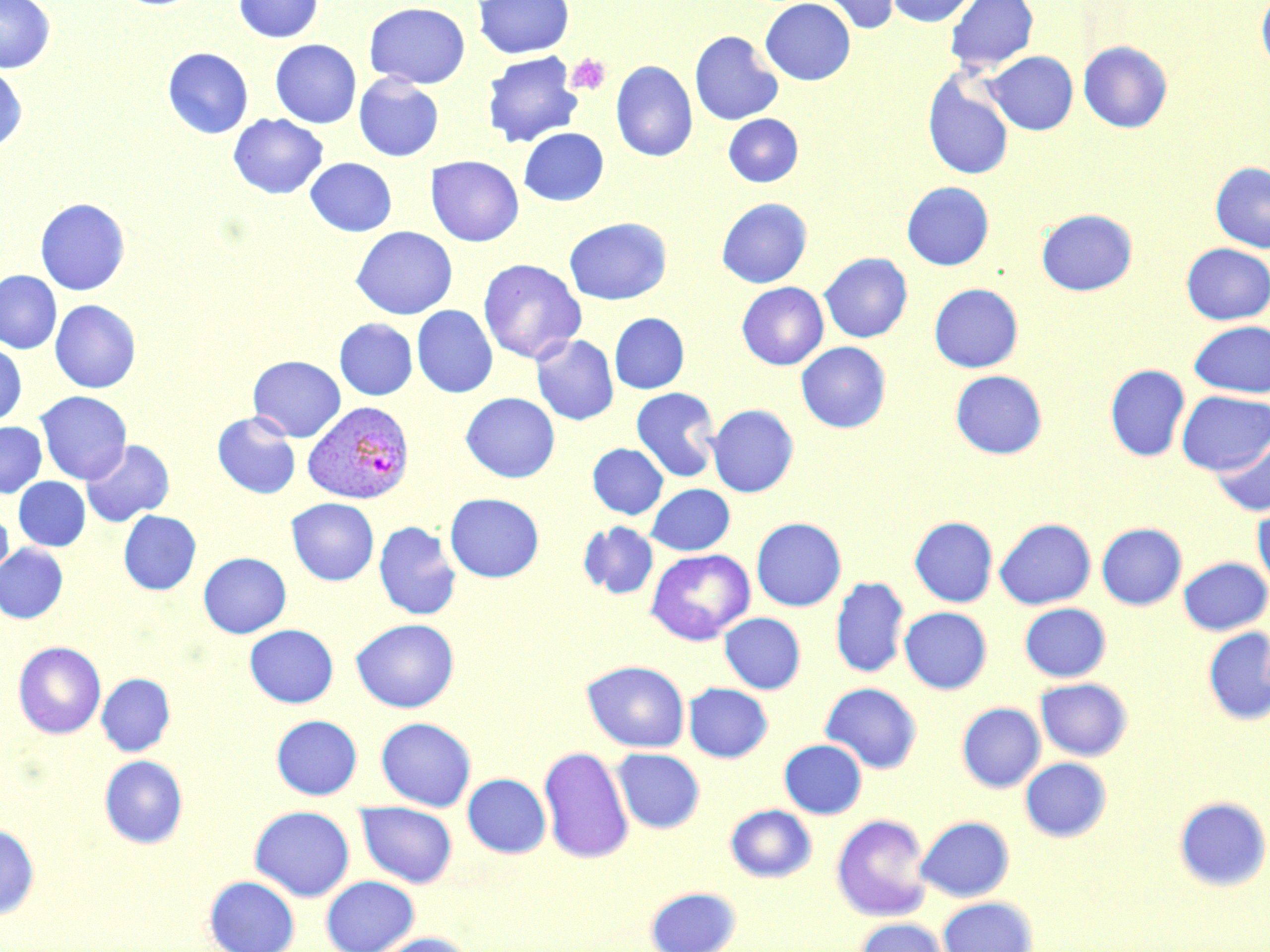
Summary:
  - Coordinate format: approximate bounding boxes as named x1/y1/x2/y2 corners in pixels
  - Platelet locations: (x1=565, y1=53, x2=612, y2=95)
  - Uninfected red blood cell locations: (x1=0, y1=0, x2=55, y2=73), (x1=232, y1=0, x2=323, y2=42), (x1=473, y1=0, x2=574, y2=58), (x1=760, y1=0, x2=855, y2=85), (x1=816, y1=0, x2=901, y2=35), (x1=885, y1=0, x2=977, y2=27), (x1=944, y1=0, x2=1039, y2=74), (x1=1256, y1=0, x2=1270, y2=72), (x1=364, y1=2, x2=471, y2=88), (x1=689, y1=30, x2=784, y2=125), (x1=270, y1=39, x2=361, y2=128), (x1=1078, y1=41, x2=1172, y2=133), (x1=163, y1=47, x2=254, y2=138), (x1=984, y1=50, x2=1078, y2=135), (x1=482, y1=52, x2=583, y2=147), (x1=611, y1=60, x2=698, y2=162), (x1=0, y1=64, x2=28, y2=152), (x1=923, y1=71, x2=1014, y2=181), (x1=354, y1=73, x2=443, y2=162), (x1=229, y1=113, x2=328, y2=199), (x1=724, y1=113, x2=803, y2=187), (x1=518, y1=127, x2=609, y2=206), (x1=426, y1=155, x2=523, y2=246), (x1=305, y1=157, x2=397, y2=236), (x1=1210, y1=161, x2=1270, y2=252), (x1=901, y1=181, x2=994, y2=270), (x1=717, y1=197, x2=812, y2=287), (x1=35, y1=198, x2=130, y2=295), (x1=1036, y1=208, x2=1137, y2=296), (x1=563, y1=218, x2=671, y2=305), (x1=352, y1=226, x2=457, y2=319), (x1=1181, y1=243, x2=1270, y2=324), (x1=819, y1=252, x2=912, y2=342), (x1=478, y1=258, x2=586, y2=364), (x1=0, y1=270, x2=61, y2=353), (x1=737, y1=282, x2=828, y2=369), (x1=929, y1=283, x2=1023, y2=372), (x1=50, y1=300, x2=140, y2=392), (x1=412, y1=305, x2=498, y2=397), (x1=610, y1=313, x2=689, y2=393), (x1=335, y1=318, x2=417, y2=400), (x1=1189, y1=320, x2=1270, y2=397), (x1=530, y1=334, x2=619, y2=425), (x1=0, y1=342, x2=27, y2=427), (x1=796, y1=342, x2=891, y2=432), (x1=248, y1=355, x2=345, y2=442), (x1=1105, y1=364, x2=1190, y2=462), (x1=950, y1=370, x2=1047, y2=458), (x1=631, y1=387, x2=720, y2=482), (x1=1176, y1=390, x2=1270, y2=475), (x1=35, y1=391, x2=131, y2=483), (x1=461, y1=392, x2=560, y2=482), (x1=707, y1=404, x2=798, y2=497), (x1=212, y1=411, x2=301, y2=499), (x1=0, y1=421, x2=46, y2=498), (x1=1209, y1=431, x2=1270, y2=516), (x1=81, y1=440, x2=174, y2=527), (x1=587, y1=443, x2=668, y2=519), (x1=14, y1=477, x2=90, y2=551), (x1=646, y1=484, x2=734, y2=555), (x1=445, y1=492, x2=544, y2=582), (x1=286, y1=498, x2=378, y2=585), (x1=1253, y1=503, x2=1270, y2=594), (x1=0, y1=509, x2=13, y2=585), (x1=118, y1=510, x2=201, y2=595), (x1=909, y1=516, x2=997, y2=607), (x1=751, y1=517, x2=846, y2=611), (x1=995, y1=518, x2=1096, y2=609), (x1=374, y1=521, x2=462, y2=620), (x1=578, y1=521, x2=659, y2=600), (x1=1096, y1=523, x2=1187, y2=610), (x1=0, y1=544, x2=67, y2=623), (x1=645, y1=548, x2=755, y2=645), (x1=198, y1=552, x2=291, y2=638), (x1=1179, y1=557, x2=1270, y2=634), (x1=830, y1=576, x2=909, y2=678), (x1=1020, y1=603, x2=1110, y2=681), (x1=899, y1=606, x2=992, y2=693), (x1=719, y1=613, x2=805, y2=693), (x1=351, y1=618, x2=459, y2=712), (x1=244, y1=624, x2=338, y2=708), (x1=1203, y1=627, x2=1270, y2=725), (x1=13, y1=641, x2=106, y2=738), (x1=582, y1=660, x2=689, y2=752), (x1=97, y1=673, x2=175, y2=756), (x1=1035, y1=678, x2=1132, y2=760), (x1=820, y1=682, x2=922, y2=773), (x1=683, y1=683, x2=773, y2=762), (x1=957, y1=703, x2=1045, y2=792), (x1=271, y1=715, x2=362, y2=800), (x1=376, y1=717, x2=476, y2=811), (x1=779, y1=739, x2=867, y2=818), (x1=539, y1=746, x2=634, y2=863), (x1=611, y1=748, x2=704, y2=833), (x1=99, y1=755, x2=188, y2=848), (x1=1020, y1=757, x2=1112, y2=841), (x1=463, y1=773, x2=550, y2=858), (x1=1174, y1=796, x2=1270, y2=891), (x1=357, y1=802, x2=457, y2=888), (x1=725, y1=804, x2=816, y2=882), (x1=249, y1=806, x2=355, y2=901), (x1=831, y1=814, x2=932, y2=921), (x1=916, y1=816, x2=1014, y2=901), (x1=0, y1=824, x2=39, y2=918), (x1=321, y1=875, x2=419, y2=951), (x1=204, y1=876, x2=299, y2=952), (x1=645, y1=886, x2=742, y2=952), (x1=938, y1=897, x2=1037, y2=952), (x1=855, y1=918, x2=951, y2=952), (x1=371, y1=933, x2=474, y2=952)
  - Plasmodium vivax-infected red blood cell locations: (x1=304, y1=400, x2=415, y2=504)
  - Slide-level diagnosis: Plasmodium vivax
  - Modality: optical microscopy
  - Stain: May-Grünwald-Giemsa
  - Magnification: 1000x
  - Field of view: single
  - Preparation: thin blood smear
  - Image size: 1270×952 pixels